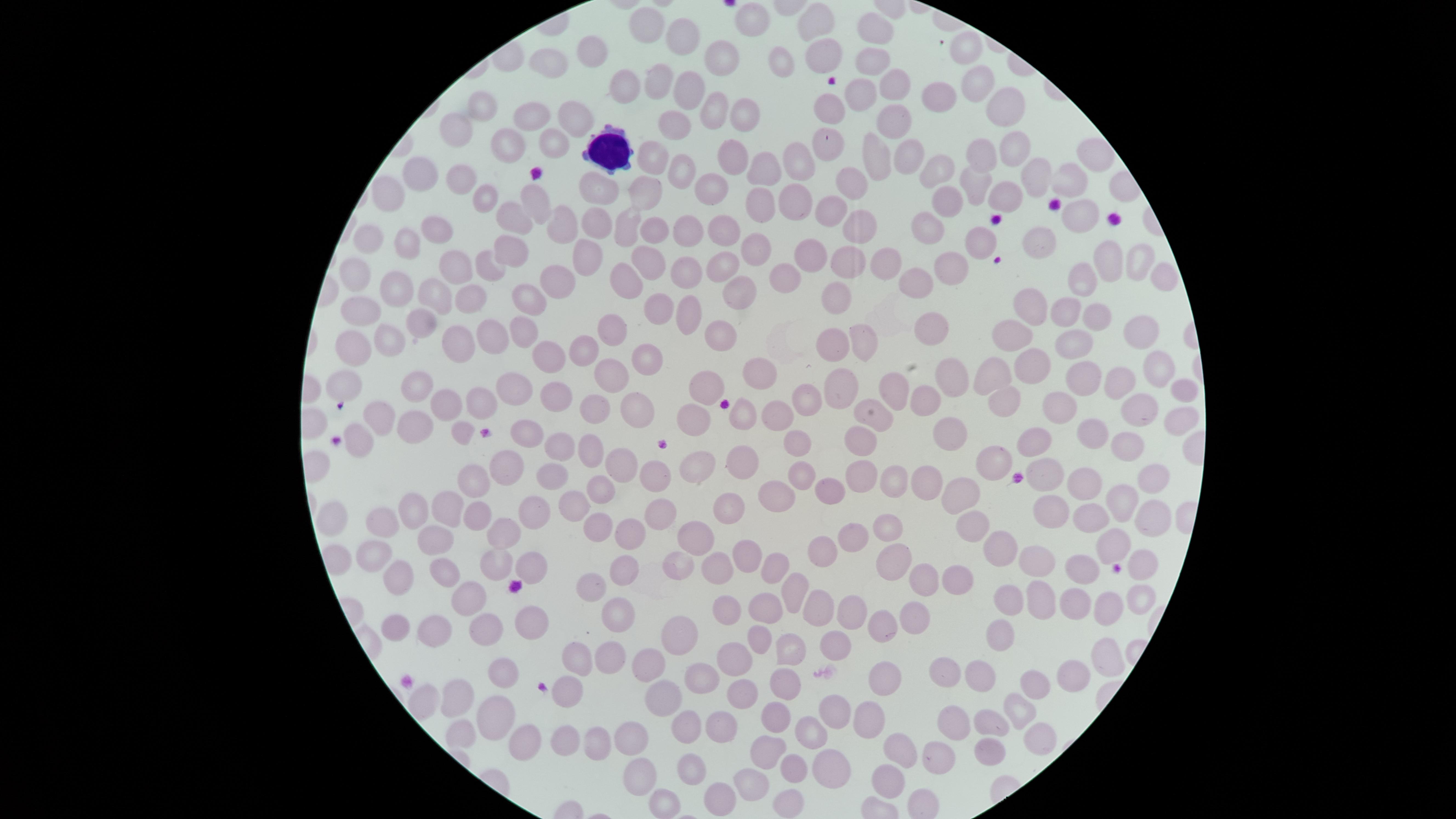
Approximate marker points as {x, y} in pixels. Uninfected red blood cells: {810, 21}, {750, 24}, {651, 30}, {878, 30}, {678, 34}, {962, 50}, {590, 52}, {816, 57}, {725, 63}, {788, 65}, {870, 67}, {545, 68}, {657, 76}, {897, 82}, {971, 85}, {625, 88}, {693, 89}, {937, 95}, {825, 96}, {867, 97}, {997, 103}, {484, 104}, {716, 111}, {742, 115}, {531, 119}, {892, 119}, {579, 121}, {671, 124}, {460, 134}, {823, 137}, {556, 141}, {510, 142}, {1010, 148}, {903, 152}, {980, 153}, {737, 155}, {799, 155}, {1092, 155}, {657, 162}, {872, 163}, {939, 165}, {679, 167}, {766, 168}, {1029, 175}, {424, 176}, {464, 176}, {1063, 184}, {977, 186}, {854, 188}, {708, 190}, {394, 194}, {648, 194}, {597, 195}, {801, 196}, {486, 198}, {949, 198}, {1005, 198}, {536, 205}, {761, 209}, {836, 209}, {1082, 214}, {596, 218}, {563, 219}, {516, 220}, {931, 222}, {680, 224}, {719, 224}, {441, 225}, {652, 228}, {854, 228}, {629, 230}, {408, 241}, {1043, 241}, {988, 243}, {362, 246}, {755, 249}, {584, 250}, {508, 253}, {650, 257}, {1138, 257}, {813, 258}, {846, 262}, {888, 263}, {1107, 263}, {493, 265}, {457, 267}, {954, 271}, {686, 272}, {717, 272}, {356, 274}, {787, 274}, {1163, 274}, {1088, 278}, {633, 279}, {551, 280}, {922, 281}, {402, 290}, {735, 292}, {433, 296}, {835, 298}, {476, 300}, {523, 303}, {660, 304}, {1033, 306}, {365, 309}, {1063, 309}, {694, 311}, {1096, 311}, {418, 321}, {607, 323}, {934, 325}, {1138, 327}, {517, 332}, {719, 332}, {490, 334}, {461, 340}, {389, 341}, {1012, 342}, {354, 343}, {854, 344}, {1069, 345}, {583, 350}, {833, 351}, {545, 356}, {643, 362}, {1033, 366}, {1156, 369}, {611, 374}, {756, 374}, {956, 374}, {999, 378}, {348, 379}, {1087, 379}, {705, 380}, {418, 381}, {511, 388}, {1122, 389}, {840, 390}, {1184, 390}, {894, 392}, {552, 393}, {485, 398}, {449, 401}, {1008, 402}, {806, 403}, {1048, 404}, {931, 405}, {1139, 405}, {647, 410}, {590, 411}, {874, 413}, {740, 415}, {697, 417}, {774, 417}, {1175, 418}, {377, 419}, {411, 425}, {457, 431}, {1091, 433}, {950, 434}, {530, 435}, {799, 442}, {859, 442}, {1041, 442}, {356, 444}, {554, 445}, {1124, 447}, {582, 448}, {694, 458}, {619, 460}, {739, 462}, {984, 462}, {505, 463}, {652, 473}, {471, 475}, {861, 475}, {1053, 475}, {795, 480}, {547, 481}, {899, 481}, {1144, 483}, {933, 484}, {1088, 486}, {833, 488}, {963, 492}, {600, 494}, {766, 496}, {574, 501}, {1117, 501}, {447, 504}, {728, 504}, {419, 509}, {654, 509}, {1044, 510}, {1144, 511}, {528, 512}, {335, 515}, {1087, 517}, {477, 521}, {379, 522}, {968, 526}, {599, 529}, {630, 530}, {889, 532}, {700, 534}, {432, 536}, {849, 539}, {503, 540}, {820, 544}, {737, 548}, {1113, 549}, {371, 551}, {1006, 554}, {1041, 559}, {678, 560}, {895, 561}, {1148, 561}, {493, 563}, {773, 563}, {443, 565}, {523, 566}, {711, 566}, {1092, 567}, {627, 569}, {395, 578}, {950, 579}, {919, 580}, {589, 587}, {788, 591}, {1138, 595}, {1033, 597}, {468, 598}, {1010, 599}, {1073, 600}, {842, 602}, {1102, 607}, {724, 608}, {814, 611}, {763, 612}, {908, 612}, {614, 620}, {483, 621}, {530, 622}, {396, 626}, {439, 626}, {884, 628}, {674, 631}, {996, 636}, {754, 641}, {830, 642}, {603, 654}, {791, 654}, {730, 658}, {576, 660}, {1088, 663}, {648, 666}, {955, 671}, {493, 674}, {982, 675}, {706, 676}, {1064, 679}, {790, 681}, {1036, 681}, {887, 682}, {463, 692}, {738, 692}, {566, 697}, {666, 698}, {422, 702}, {1019, 705}, {830, 710}, {487, 711}, {778, 716}, {868, 716}, {958, 721}, {992, 722}, {460, 725}, {714, 725}, {683, 729}, {808, 732}, {1036, 735}, {592, 736}, {564, 737}, {627, 737}, {525, 744}, {768, 746}, {985, 746}, {897, 754}, {935, 758}, {792, 762}, {690, 763}, {825, 769}, {635, 778}, {884, 780}, {751, 784}, {719, 799}, {788, 800}, {661, 805}. White blood cells: {614, 153}. Thin blood film. Single field of view. Image is 1456×819 pixels. Smartphone photograph through the microscope eyepiece. Giemsa-stained preparation. Presence: no malaria parasites identified. Circular visible region.